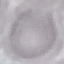
Summary:
  - Malaria status: uninfected
  - Stain: Giemsa
  - Preparation: thin blood smear
  - Image type: automatically extracted cell patch, resized to 64 × 64 pixels
  - Capture: smartphone through the microscope eyepiece